Outline each blood parasite and name the species.
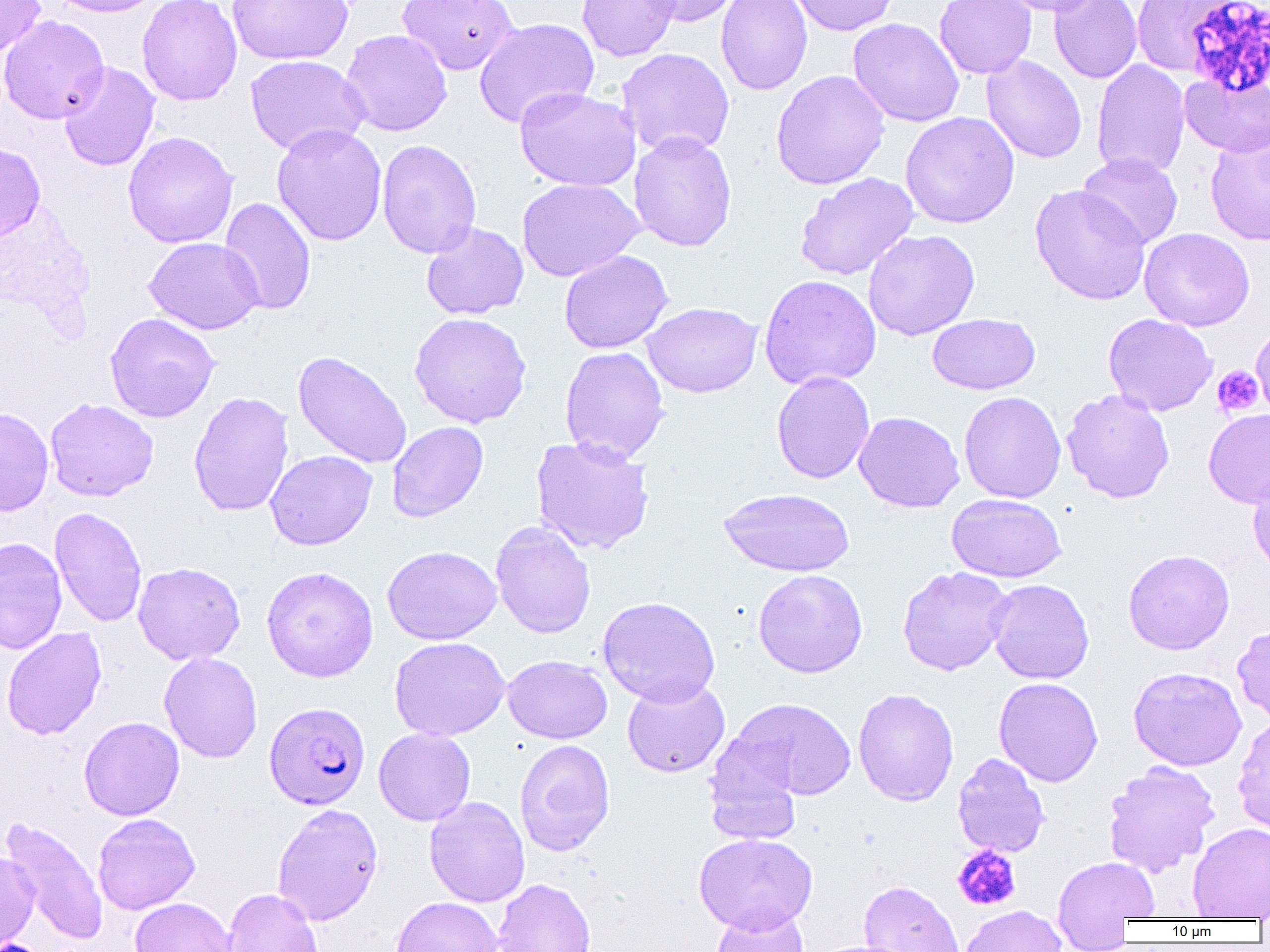

Approximate bounding boxes as (x1, y1, x2, y2) in pixels.
Plasmodium falciparum-infected red blood cells: (264, 702, 370, 809).
No Plasmodium ovale, Plasmodium malariae, Plasmodium vivax, Babesia divergens, or Trypanosoma brucei observed.

Summary:
  - Platelet locations: (1211, 365, 1265, 418), (952, 845, 1020, 911)
  - Uninfected red blood cell locations: (0, 0, 46, 56), (47, 0, 166, 17), (136, 0, 242, 105), (227, 0, 353, 65), (397, 0, 519, 76), (577, 0, 680, 62), (640, 0, 741, 26), (716, 0, 812, 95), (787, 0, 899, 36), (934, 0, 1037, 79), (996, 0, 1106, 16), (1049, 0, 1142, 83), (1130, 0, 1239, 77), (0, 15, 109, 124), (473, 18, 599, 129), (848, 18, 965, 127), (340, 29, 452, 136), (617, 48, 735, 158), (245, 54, 369, 156), (982, 54, 1087, 164), (1091, 59, 1190, 179), (58, 62, 160, 172), (770, 70, 889, 190), (1180, 72, 1270, 158), (514, 86, 639, 192), (900, 112, 1019, 228), (272, 123, 387, 246), (123, 131, 238, 249), (628, 131, 737, 252), (1204, 133, 1270, 246), (377, 139, 482, 259), (0, 142, 46, 243), (1077, 152, 1183, 249), (795, 172, 918, 281), (516, 178, 644, 282), (1029, 185, 1151, 305), (218, 197, 316, 316), (421, 222, 528, 320), (1139, 227, 1255, 331), (863, 229, 980, 340), (144, 237, 264, 334), (559, 250, 673, 353), (759, 274, 882, 390), (641, 302, 762, 398), (105, 312, 220, 422), (409, 312, 531, 428), (927, 313, 1040, 395), (1103, 313, 1217, 416), (1251, 325, 1270, 419), (560, 346, 670, 464), (292, 350, 412, 469), (771, 371, 875, 484), (1061, 388, 1175, 503), (188, 391, 294, 517), (959, 391, 1066, 503), (44, 398, 159, 502), (0, 407, 54, 516), (1203, 408, 1270, 508), (853, 411, 964, 513), (387, 421, 488, 522), (530, 435, 654, 554), (265, 450, 377, 551), (1248, 471, 1270, 576), (718, 488, 854, 577), (947, 494, 1066, 582), (50, 506, 147, 627), (490, 521, 596, 638), (0, 538, 67, 655), (382, 545, 502, 645), (1123, 549, 1234, 655), (133, 562, 245, 665), (261, 566, 379, 682), (897, 566, 1014, 676), (753, 569, 868, 678), (986, 579, 1094, 684), (597, 596, 720, 706), (1233, 624, 1270, 726), (1, 626, 107, 740), (389, 636, 510, 741), (159, 653, 263, 763), (502, 655, 612, 743), (1128, 666, 1247, 771), (622, 677, 730, 777), (993, 677, 1103, 786), (853, 688, 959, 806), (731, 698, 856, 801), (1233, 715, 1270, 836), (79, 716, 184, 820), (374, 727, 476, 825), (515, 739, 615, 856), (703, 748, 804, 846), (952, 753, 1050, 858), (1102, 761, 1221, 878), (424, 796, 530, 907), (272, 803, 384, 925), (93, 813, 200, 915), (2, 816, 109, 944), (1188, 822, 1270, 919), (694, 833, 817, 933), (0, 850, 40, 950), (1052, 855, 1160, 938), (493, 879, 595, 952), (858, 880, 965, 952), (223, 887, 323, 952), (390, 896, 503, 952), (130, 897, 237, 952), (710, 904, 809, 952), (959, 905, 1067, 952), (810, 940, 919, 952)
  - Slide-level diagnosis: Plasmodium falciparum
  - Modality: light microscopy
  - Preparation: thin blood smear
  - Image size: 1270×952 pixels
  - Field of view: one of a larger specimen
  - Magnification: 1000x